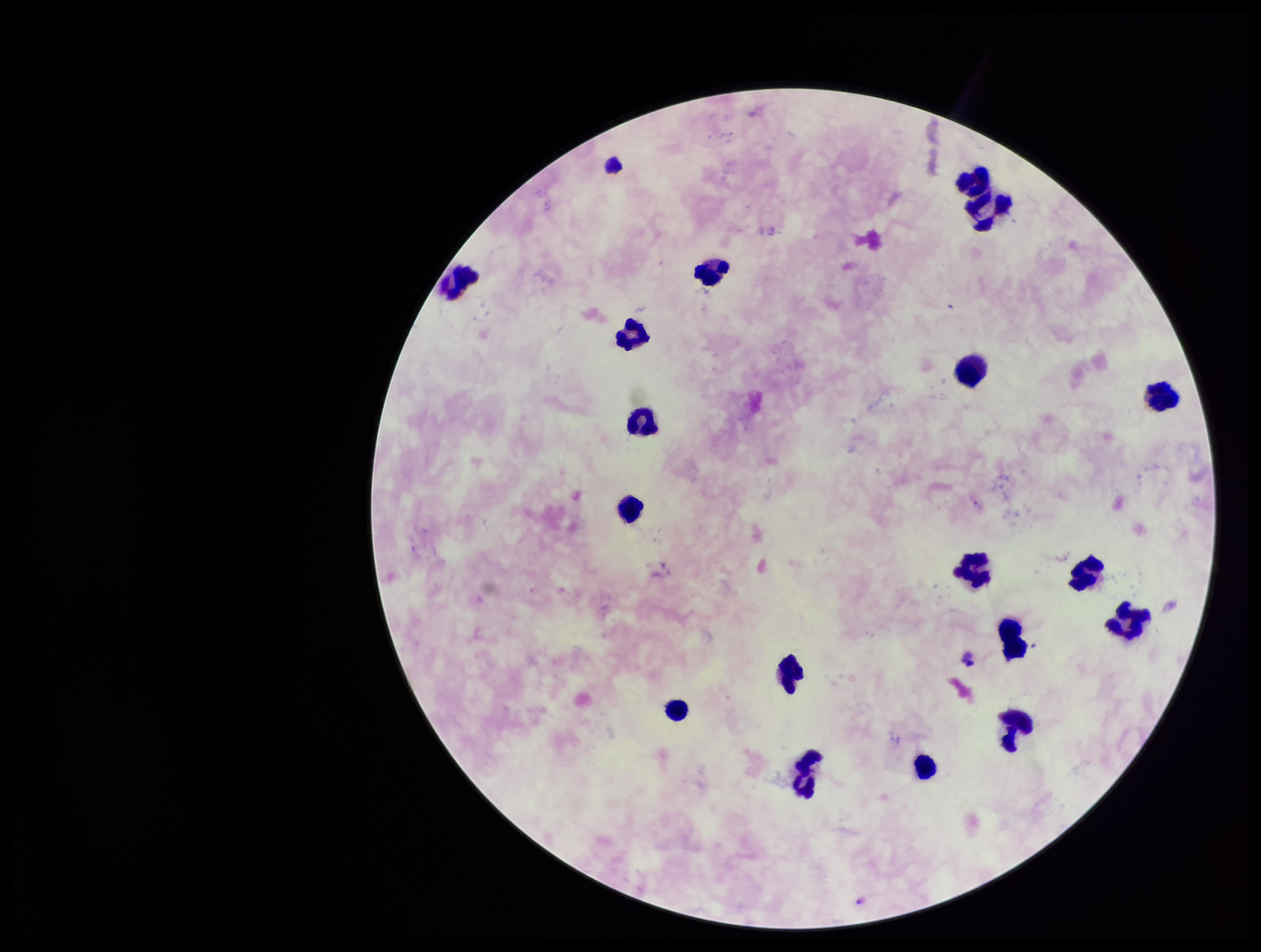

patient_malaria_status: negative
plasmodium_parasites: none seen
capture: smartphone photograph through the microscope eyepiece
leukocyte_count: 18
image_size: 1261×952 pixels
preparation: thick
field_of_view: single
parasite_count: 0
stain: Giemsa